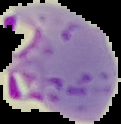 From a thin blood smear. Segmented cell region on a black background. Result: Plasmodium parasites detected. Image is 121×124 pixels.